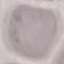

result = negative for malaria parasites
stain = Giemsa
image type = automatically extracted cell patch, resized to 64 × 64 pixels
capture = smartphone camera at the microscope eyepiece
preparation = thin blood film